Classify this cell by malaria status.
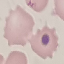
Uninfected.

capture = smartphone camera at the microscope eyepiece
stain = Giemsa
preparation = thin smear
image type = automatically extracted cell patch, resized to 64 × 64 pixels